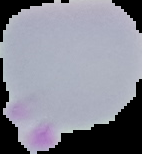

Summary:
  - Malaria status: uninfected
  - Image type: segmented cell region with the area outside set to black
  - Image size: 142×154 pixels
  - Preparation: thin blood film